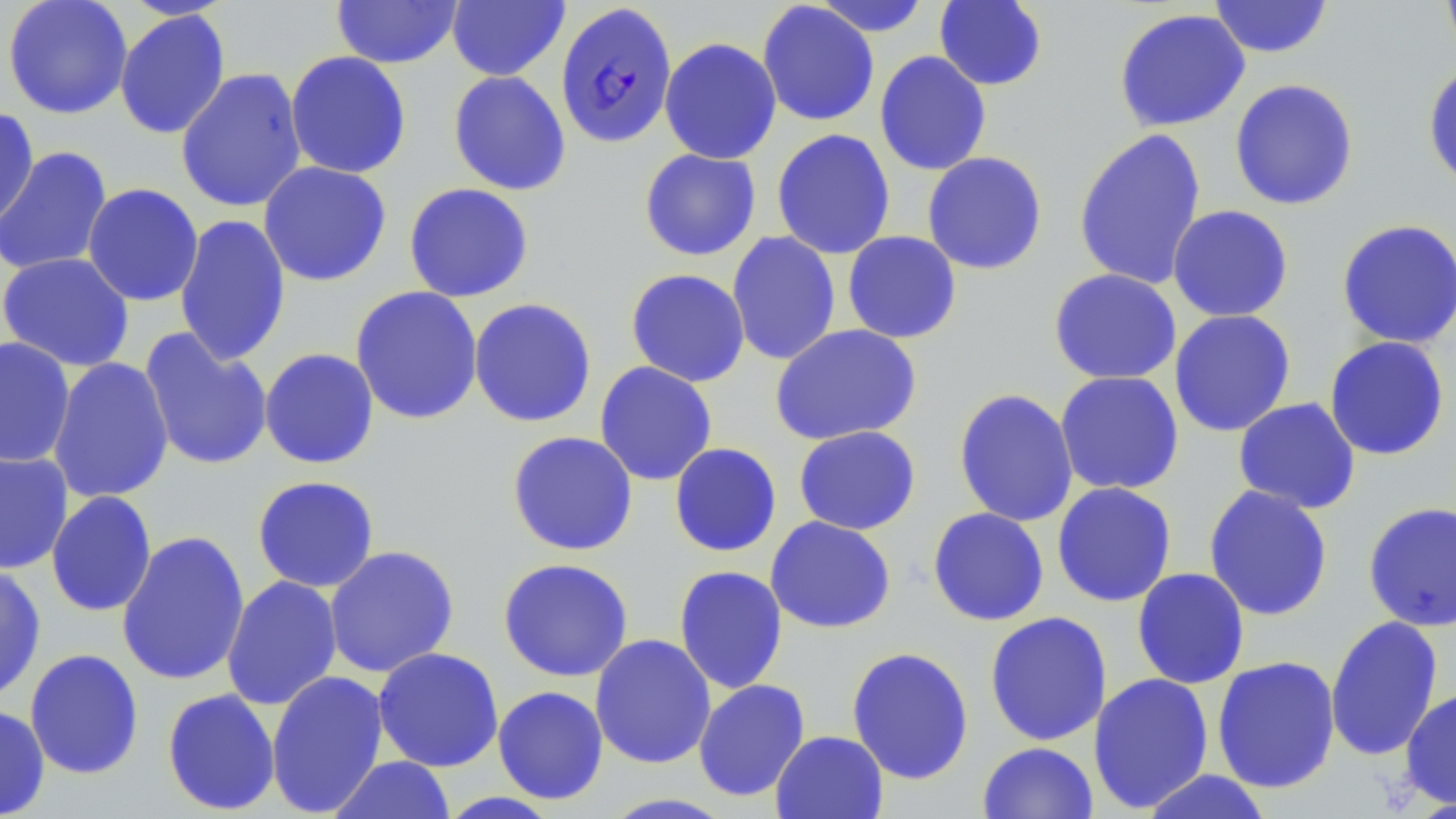

slide_level_diagnosis: Plasmodium falciparum
field_of_view: single
magnification: 1000x
modality: light microscopy
preparation: thin blood smear
image_size: 1456×819 pixels
plasmodium_falciparum_infected_red_blood_cell_locations: 'approximate bounding boxes as named x1/y1/x2/y2 corners in pixels: (x1=555, y1=2, x2=678, y2=149)'
uninfected_red_blood_cell_locations: 'approximate bounding boxes as named x1/y1/x2/y2 corners in pixels: (x1=2, y1=0, x2=133, y2=119), (x1=331, y1=0, x2=464, y2=69), (x1=446, y1=0, x2=570, y2=82), (x1=809, y1=0, x2=933, y2=37), (x1=933, y1=0, x2=1048, y2=91), (x1=1207, y1=0, x2=1334, y2=59), (x1=1440, y1=0, x2=1456, y2=64), (x1=756, y1=1, x2=880, y2=127), (x1=114, y1=8, x2=231, y2=140), (x1=1113, y1=8, x2=1251, y2=132), (x1=659, y1=36, x2=782, y2=165), (x1=284, y1=50, x2=412, y2=179), (x1=874, y1=50, x2=992, y2=176), (x1=1422, y1=61, x2=1456, y2=190), (x1=175, y1=67, x2=308, y2=213), (x1=447, y1=70, x2=572, y2=196), (x1=1228, y1=78, x2=1360, y2=211), (x1=0, y1=106, x2=40, y2=231), (x1=771, y1=128, x2=896, y2=260), (x1=1072, y1=128, x2=1208, y2=291), (x1=0, y1=145, x2=112, y2=278), (x1=638, y1=148, x2=761, y2=261), (x1=921, y1=151, x2=1048, y2=275), (x1=258, y1=161, x2=392, y2=287), (x1=81, y1=182, x2=204, y2=307), (x1=403, y1=182, x2=534, y2=303), (x1=1167, y1=205, x2=1294, y2=322), (x1=174, y1=213, x2=291, y2=367), (x1=1335, y1=218, x2=1456, y2=349), (x1=842, y1=230, x2=962, y2=344), (x1=726, y1=231, x2=841, y2=366), (x1=0, y1=252, x2=135, y2=372), (x1=625, y1=268, x2=751, y2=388), (x1=1048, y1=268, x2=1182, y2=385), (x1=350, y1=285, x2=483, y2=425), (x1=468, y1=297, x2=598, y2=428), (x1=1169, y1=309, x2=1296, y2=437), (x1=770, y1=323, x2=922, y2=446), (x1=138, y1=328, x2=274, y2=471), (x1=0, y1=336, x2=75, y2=468), (x1=1323, y1=336, x2=1451, y2=461), (x1=259, y1=348, x2=380, y2=469), (x1=48, y1=357, x2=174, y2=504), (x1=594, y1=361, x2=718, y2=486), (x1=1054, y1=370, x2=1184, y2=495), (x1=953, y1=388, x2=1079, y2=527), (x1=1233, y1=397, x2=1361, y2=514), (x1=793, y1=425, x2=922, y2=535), (x1=506, y1=430, x2=639, y2=556), (x1=669, y1=442, x2=782, y2=557), (x1=0, y1=449, x2=74, y2=575), (x1=251, y1=475, x2=380, y2=593), (x1=1051, y1=481, x2=1177, y2=607), (x1=1203, y1=484, x2=1333, y2=621), (x1=45, y1=490, x2=158, y2=617), (x1=1362, y1=501, x2=1456, y2=632), (x1=927, y1=507, x2=1050, y2=626), (x1=765, y1=516, x2=897, y2=634), (x1=116, y1=529, x2=250, y2=688), (x1=323, y1=545, x2=460, y2=678), (x1=496, y1=557, x2=634, y2=682), (x1=0, y1=562, x2=46, y2=705), (x1=673, y1=565, x2=788, y2=695), (x1=1131, y1=567, x2=1250, y2=690), (x1=221, y1=575, x2=343, y2=711), (x1=984, y1=611, x2=1113, y2=746), (x1=1324, y1=615, x2=1444, y2=761), (x1=590, y1=634, x2=716, y2=769), (x1=372, y1=646, x2=504, y2=772), (x1=846, y1=646, x2=975, y2=785), (x1=24, y1=648, x2=144, y2=780), (x1=1211, y1=655, x2=1341, y2=794), (x1=266, y1=669, x2=389, y2=816), (x1=1088, y1=672, x2=1215, y2=813), (x1=693, y1=678, x2=811, y2=803), (x1=492, y1=685, x2=609, y2=805), (x1=1400, y1=686, x2=1456, y2=810), (x1=161, y1=687, x2=281, y2=816), (x1=0, y1=704, x2=50, y2=818), (x1=770, y1=730, x2=888, y2=819), (x1=977, y1=741, x2=1099, y2=819), (x1=327, y1=755, x2=456, y2=818), (x1=1139, y1=769, x2=1274, y2=819), (x1=435, y1=791, x2=564, y2=818), (x1=598, y1=792, x2=738, y2=818)'
stain: May-Grünwald-Giemsa